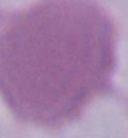

modality: photomicrograph
identification: red blood cell
magnification: 1000x